Outline each Plasmodium falciparum-infected red blood cell.
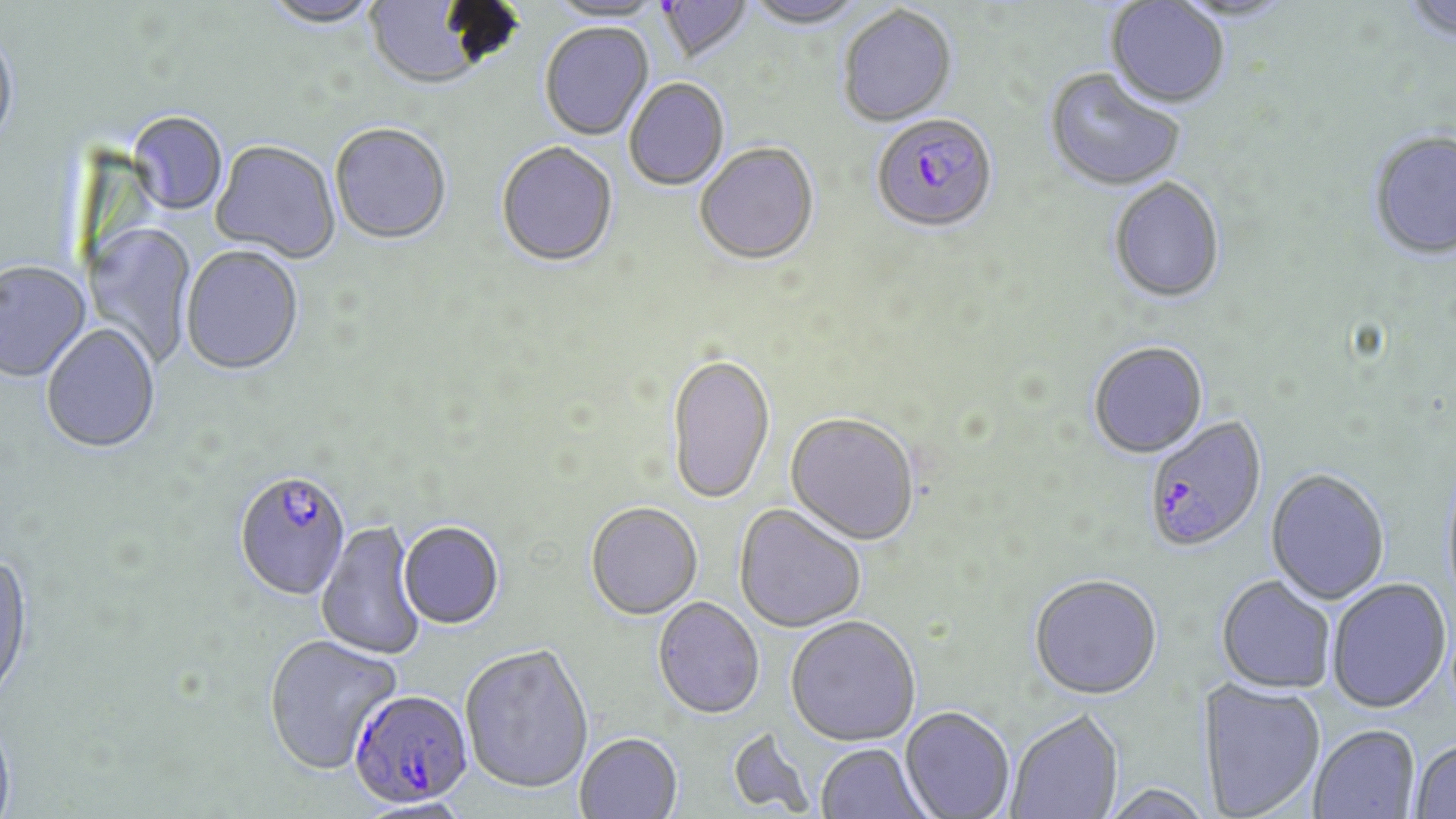

Approximate bounding boxes as named x1/y1/x2/y2 corners in pixels.
Plasmodium falciparum-infected red blood cells: (x1=871, y1=116, x2=998, y2=236), (x1=1144, y1=414, x2=1267, y2=552), (x1=234, y1=471, x2=353, y2=603), (x1=349, y1=689, x2=474, y2=808).

slide_level_diagnosis: Plasmodium falciparum
uninfected_red_blood_cell_locations: 'approximate bounding boxes as named x1/y1/x2/y2 corners in pixels: (x1=262, y1=0, x2=382, y2=29), (x1=744, y1=0, x2=867, y2=31), (x1=1402, y1=0, x2=1456, y2=43), (x1=364, y1=1, x2=499, y2=93), (x1=546, y1=1, x2=666, y2=26), (x1=657, y1=1, x2=754, y2=66), (x1=1104, y1=1, x2=1230, y2=110), (x1=838, y1=7, x2=958, y2=128), (x1=539, y1=24, x2=654, y2=142), (x1=0, y1=28, x2=20, y2=151), (x1=1044, y1=70, x2=1185, y2=193), (x1=625, y1=80, x2=729, y2=192), (x1=126, y1=113, x2=228, y2=217), (x1=330, y1=124, x2=452, y2=247), (x1=1369, y1=129, x2=1456, y2=259), (x1=211, y1=141, x2=340, y2=264), (x1=496, y1=143, x2=618, y2=269), (x1=695, y1=144, x2=820, y2=268), (x1=1109, y1=178, x2=1226, y2=304), (x1=84, y1=221, x2=197, y2=367), (x1=180, y1=247, x2=304, y2=377), (x1=0, y1=262, x2=90, y2=383), (x1=41, y1=325, x2=161, y2=456), (x1=1088, y1=341, x2=1209, y2=459), (x1=666, y1=353, x2=775, y2=506), (x1=785, y1=412, x2=920, y2=545), (x1=1265, y1=468, x2=1391, y2=605), (x1=586, y1=502, x2=703, y2=620), (x1=734, y1=503, x2=867, y2=633), (x1=398, y1=521, x2=504, y2=630), (x1=316, y1=522, x2=427, y2=661), (x1=0, y1=551, x2=35, y2=707), (x1=1029, y1=573, x2=1163, y2=698), (x1=1216, y1=575, x2=1336, y2=693), (x1=1327, y1=578, x2=1451, y2=713), (x1=653, y1=597, x2=764, y2=719), (x1=785, y1=615, x2=921, y2=745), (x1=263, y1=634, x2=402, y2=775), (x1=460, y1=643, x2=594, y2=794), (x1=1197, y1=678, x2=1326, y2=818), (x1=900, y1=705, x2=1015, y2=818), (x1=1006, y1=708, x2=1123, y2=818), (x1=0, y1=719, x2=18, y2=819), (x1=1309, y1=723, x2=1420, y2=818), (x1=575, y1=732, x2=683, y2=819), (x1=1410, y1=737, x2=1456, y2=817), (x1=815, y1=743, x2=931, y2=819)'
preparation: thin blood smear
field_of_view: one of a larger specimen
modality: light microscopy
magnification: 1000x
image_size: 1456×819 pixels
stain: May-Grünwald-Giemsa